Name the parasite shown.
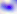

This is Toxoplasma gondii.

Summary:
  - Magnification: 400x
  - Modality: micrograph